Identify the parasite.
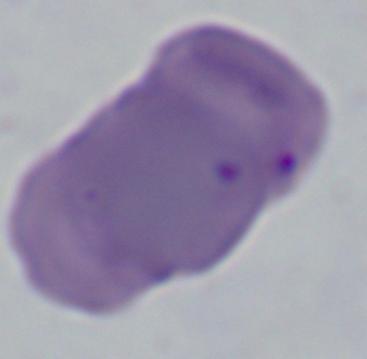

This is Babesia.

{
  "magnification": "1000x",
  "modality": "micrograph"
}